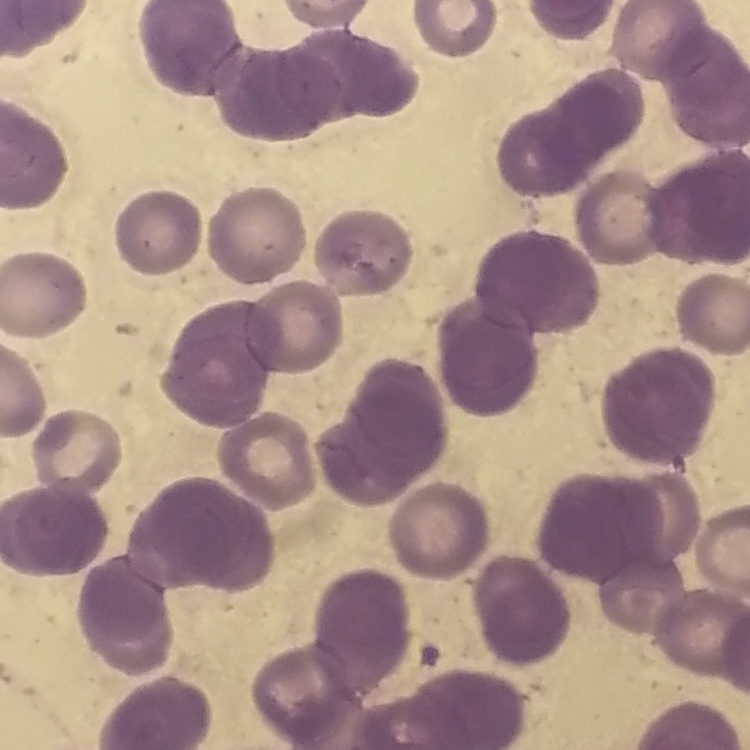
{
  "erythrocyte_morphology": "rouleaux formation",
  "preparation": "thin blood smear",
  "image_type": "one tile cut from a larger photomicrograph",
  "stain": "Field's or Giemsa"
}